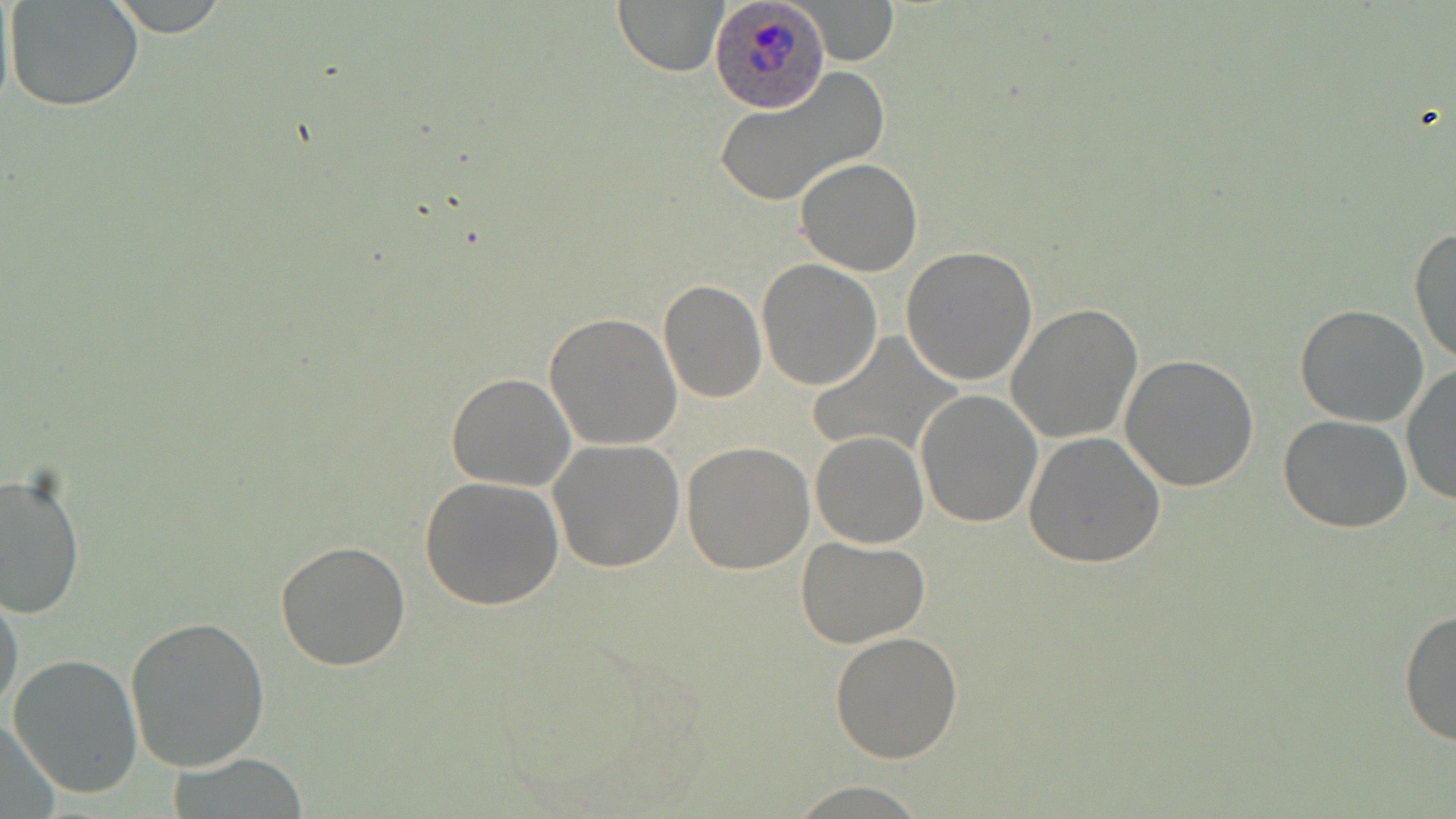
Summary:
  - Coordinate format: approximate bounding boxes as [x1, y1, x2, y2] in pixels
  - Uninfected red blood cell locations: [4, 0, 144, 113], [612, 0, 729, 75], [803, 1, 897, 65], [712, 71, 891, 206], [795, 157, 924, 276], [1408, 223, 1456, 369], [901, 246, 1038, 386], [756, 258, 884, 391], [659, 281, 765, 402], [1007, 304, 1142, 443], [1295, 305, 1429, 427], [544, 312, 682, 450], [806, 332, 964, 458], [1120, 353, 1259, 491], [1400, 364, 1456, 508], [446, 372, 576, 491], [914, 388, 1042, 528], [1278, 415, 1413, 533], [810, 431, 928, 548], [1023, 431, 1166, 569], [548, 439, 684, 574], [682, 441, 815, 574], [0, 468, 85, 620], [421, 477, 565, 610], [796, 537, 930, 648], [275, 539, 411, 669], [0, 586, 25, 720], [1400, 606, 1456, 747], [124, 614, 271, 772], [829, 631, 963, 761], [6, 653, 145, 800], [1, 711, 60, 813], [169, 754, 311, 817], [784, 781, 934, 816]
  - Plasmodium ovale-infected red blood cell locations: [709, 0, 830, 113]
  - Slide-level diagnosis: Plasmodium ovale
  - Preparation: thin blood film
  - Stain: May-Grünwald-Giemsa
  - Image size: 1456×819 pixels
  - Field of view: one of a larger specimen
  - Modality: optical microscopy
  - Magnification: 1000x